Report the malaria status of this cell.
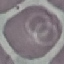
It is uninfected.

capture: smartphone camera at the microscope eyepiece
preparation: thin smear
stain: Giemsa
image_type: cell patch, automatically extracted from a larger field of view and resized to 64 × 64 pixels